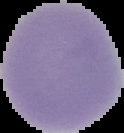

Cell region segmented out of the field of view; the surrounding area is masked to black. Image is 124×133 pixels. Result: no malaria parasites detected. From a thin blood film.